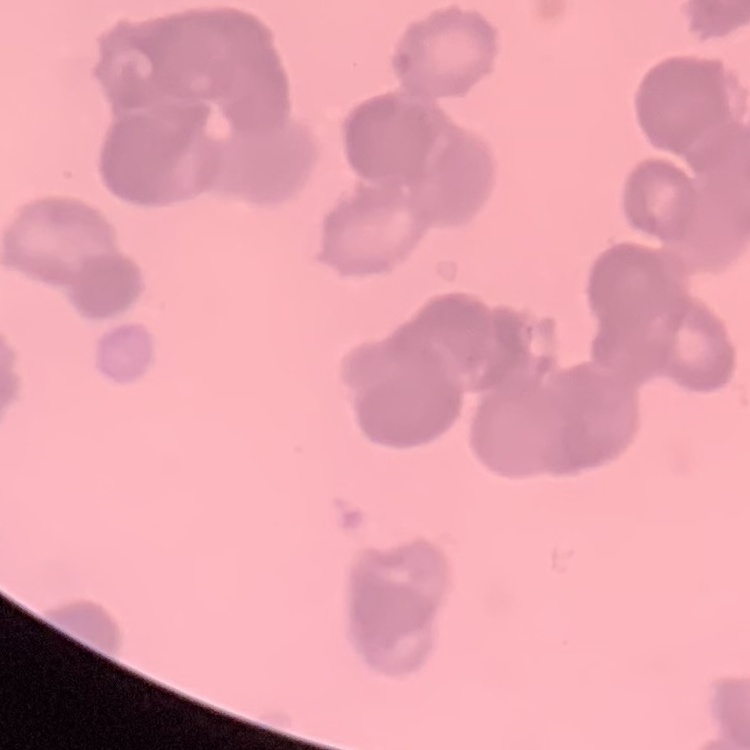
Summary:
  - Erythrocyte morphology: rouleaux formation
  - Preparation: thin blood smear
  - Image type: square crop of a larger photomicrograph
  - Stain: Field's or Giemsa